State which parasite is depicted.
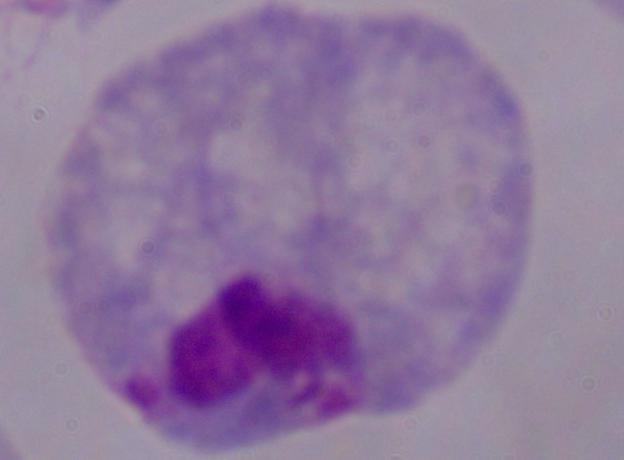

This is a trichomonad.

Summary:
  - Magnification: 1000x
  - Modality: photomicrograph